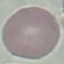
{
  "result": "negative for malaria parasites",
  "preparation": "thin blood film",
  "image_type": "automatically extracted cell patch, resized to 64 × 64 pixels",
  "capture": "smartphone camera at the microscope eyepiece",
  "stain": "Giemsa"
}